Assess for malaria.
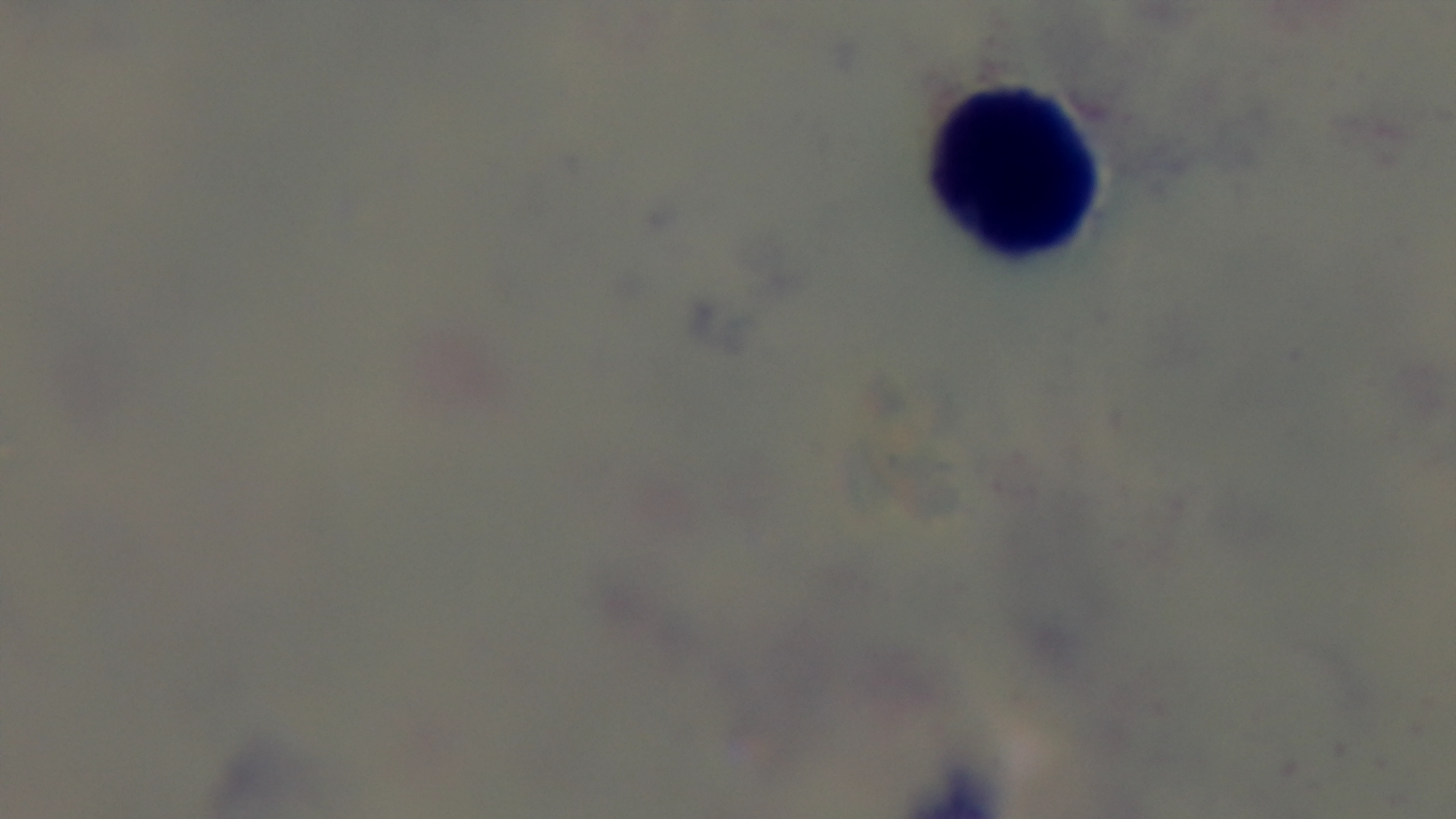
It is uninfected.

Preparation: thick smear. 100x oil-immersion objective. Giemsa-stained. Photomicrograph. One field from the slide. Captured with a mounted 4K digital camera.